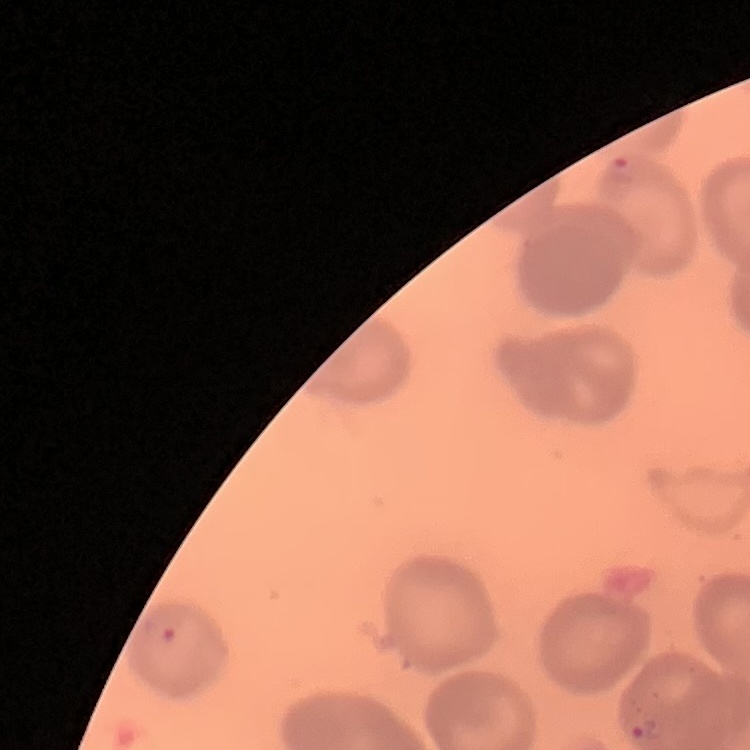
Summary:
  - Erythrocyte morphology: no rouleaux formation
  - Stain: Field's or Giemsa
  - Image type: one tile cut from a larger photomicrograph
  - Preparation: thin blood smear